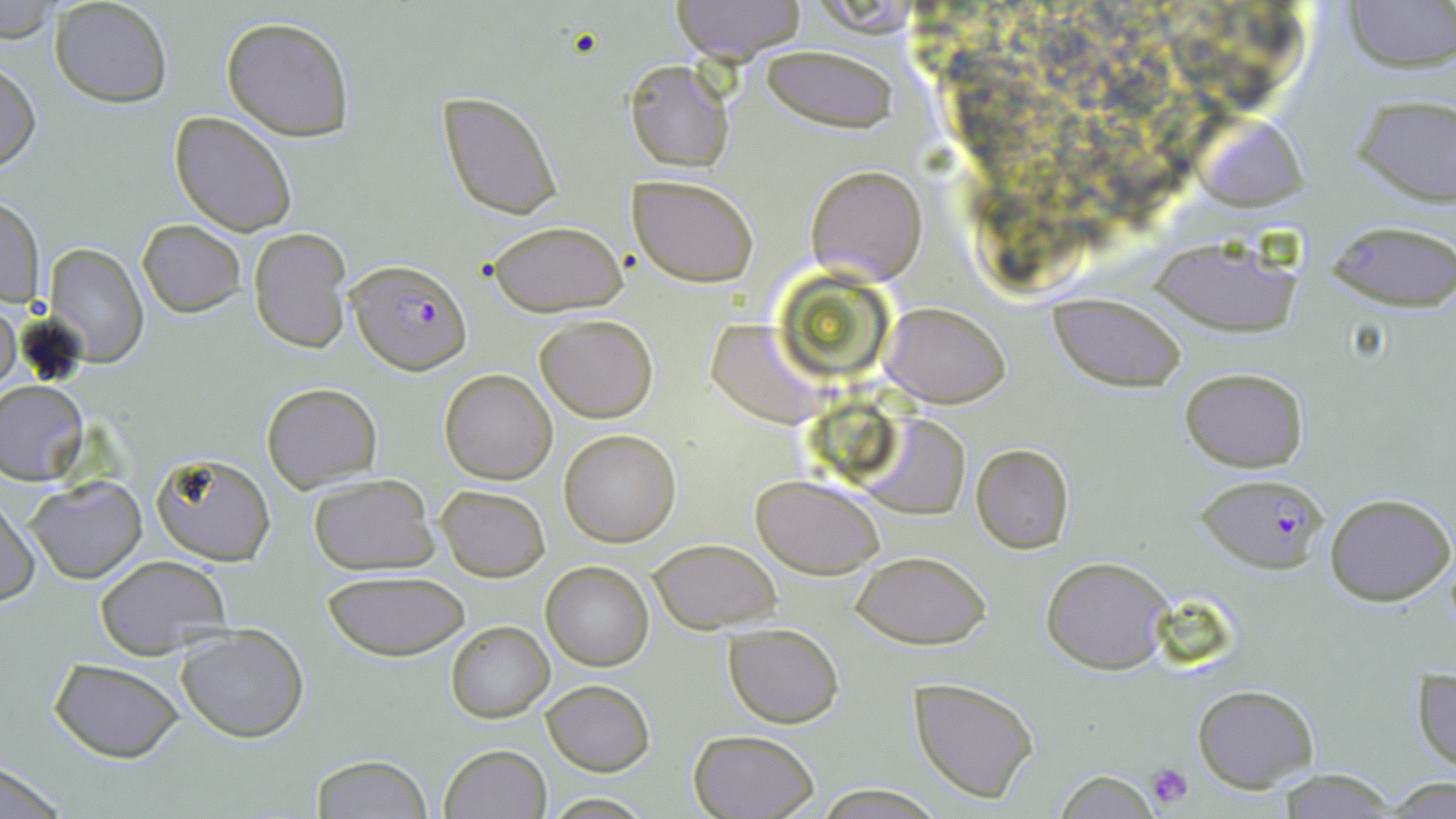
Summary:
  - Coordinate format: approximate bounding boxes as (x1, y1, x2, y2) in pixels
  - Uninfected red blood cell locations: (51, 0, 172, 108), (669, 0, 808, 65), (1343, 0, 1454, 71), (0, 2, 59, 41), (221, 16, 356, 141), (760, 43, 898, 133), (0, 60, 41, 174), (627, 62, 733, 173), (438, 90, 563, 220), (1352, 96, 1456, 206), (169, 112, 298, 237), (1198, 116, 1310, 211), (806, 165, 926, 283), (629, 174, 758, 287), (0, 196, 45, 306), (1326, 218, 1456, 311), (138, 220, 246, 318), (486, 220, 626, 316), (248, 227, 352, 353), (1148, 237, 1302, 333), (46, 244, 148, 366), (1050, 294, 1185, 392), (0, 300, 21, 394), (883, 303, 1010, 407), (537, 314, 656, 422), (707, 321, 829, 427), (1178, 366, 1309, 473), (440, 368, 558, 484), (0, 381, 89, 483), (261, 382, 382, 491), (862, 415, 971, 518), (559, 428, 681, 546), (971, 443, 1075, 553), (151, 453, 275, 567), (308, 474, 439, 574), (753, 474, 886, 579), (28, 475, 145, 583), (436, 485, 549, 582), (1325, 492, 1454, 607), (0, 495, 39, 608), (647, 539, 781, 633), (852, 550, 991, 648), (95, 555, 231, 659), (1042, 556, 1173, 674), (540, 561, 653, 670), (323, 572, 470, 662), (446, 621, 554, 722), (176, 623, 309, 743), (723, 623, 845, 728), (50, 659, 186, 763), (1412, 667, 1455, 776), (909, 677, 1040, 803), (541, 680, 654, 775), (1192, 684, 1319, 791), (687, 729, 820, 819), (438, 744, 551, 819), (310, 755, 435, 818), (0, 764, 71, 817), (1272, 768, 1400, 819), (1053, 770, 1164, 817), (1379, 776, 1456, 816), (815, 787, 949, 817), (543, 794, 655, 817)
  - Plasmodium falciparum-infected red blood cell locations: (347, 259, 471, 374), (1195, 473, 1332, 572)
  - Platelet locations: (1146, 762, 1195, 808)
  - Slide-level diagnosis: Plasmodium falciparum
  - Image size: 1456×819 pixels
  - Stain: May-Grünwald-Giemsa
  - Modality: optical microscopy
  - Field of view: single
  - Preparation: thin blood smear
  - Magnification: 1000x